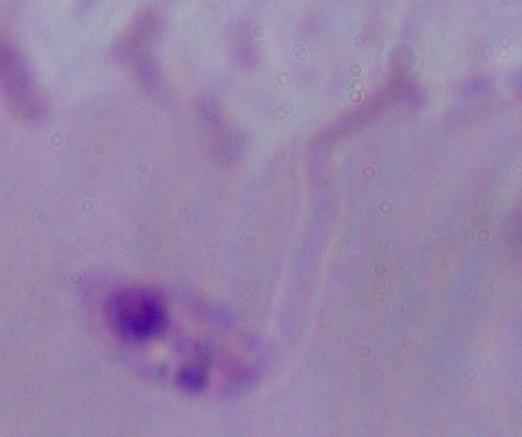
1000x magnification. A Leishmania parasite is shown. Micrograph.